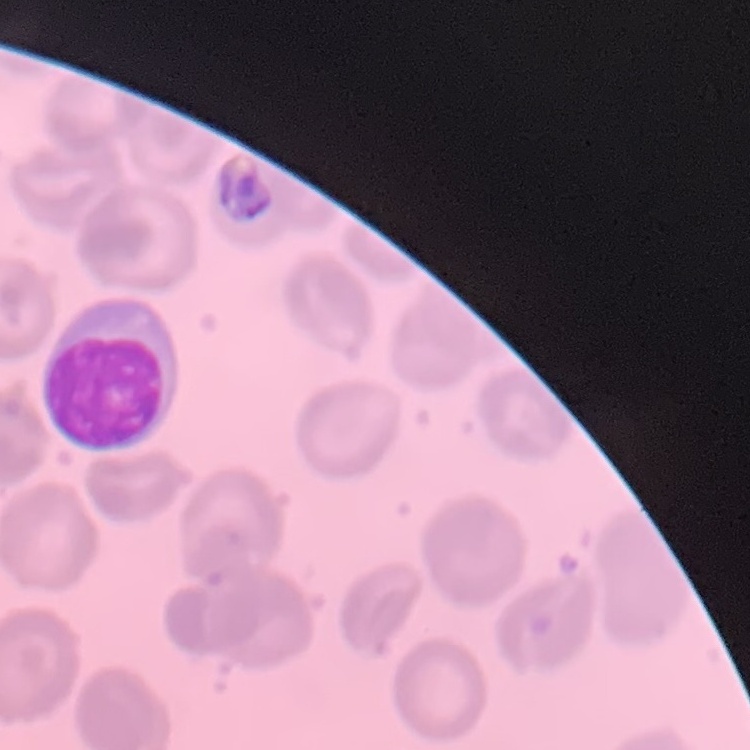
erythrocyte morphology = no rouleaux formation
stain = Field's or Giemsa
preparation = thin peripheral smear
image type = square crop of a larger photomicrograph